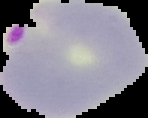 Segmented cell region on a black background. Result: malaria parasites identified. From a thin blood film. Image is 148×118 pixels.